State the blood parasite species.
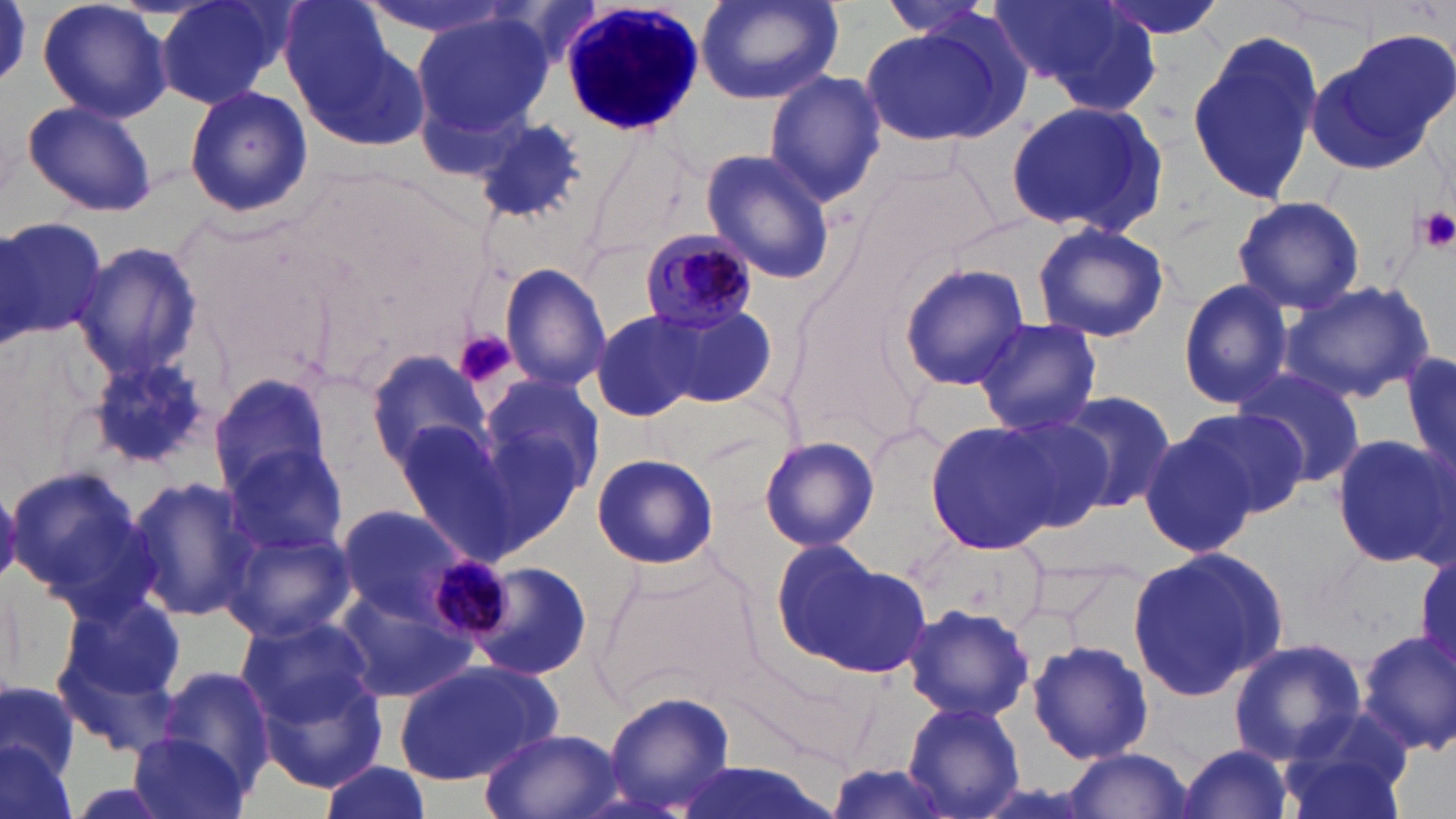

Plasmodium malariae.

field of view = single
magnification = 1000x
white blood cell locations = approximate bounding boxes as named x1/y1/x2/y2 corners in pixels: (x1=556, y1=1, x2=705, y2=140)
platelet locations = approximate bounding boxes as named x1/y1/x2/y2 corners in pixels: (x1=1415, y1=207, x2=1456, y2=254), (x1=455, y1=330, x2=516, y2=388)
preparation = thin blood smear
Plasmodium malariae-infected red blood cell locations = approximate bounding boxes as named x1/y1/x2/y2 corners in pixels: (x1=638, y1=228, x2=763, y2=335)
image size = 1456×819 pixels
uninfected red blood cell locations = approximate bounding boxes as named x1/y1/x2/y2 corners in pixels: (x1=37, y1=0, x2=173, y2=123), (x1=155, y1=0, x2=291, y2=108), (x1=696, y1=0, x2=844, y2=106), (x1=992, y1=0, x2=1161, y2=114), (x1=1093, y1=0, x2=1230, y2=43), (x1=874, y1=1, x2=1003, y2=38), (x1=411, y1=9, x2=554, y2=141), (x1=286, y1=10, x2=431, y2=149), (x1=858, y1=22, x2=1014, y2=150), (x1=1185, y1=27, x2=1322, y2=206), (x1=1310, y1=33, x2=1453, y2=174), (x1=763, y1=68, x2=887, y2=207), (x1=184, y1=86, x2=312, y2=215), (x1=22, y1=98, x2=156, y2=216), (x1=1005, y1=100, x2=1169, y2=238), (x1=468, y1=116, x2=588, y2=221), (x1=700, y1=150, x2=838, y2=285), (x1=853, y1=157, x2=997, y2=282), (x1=1231, y1=194, x2=1366, y2=316), (x1=0, y1=214, x2=106, y2=346), (x1=1032, y1=222, x2=1170, y2=343), (x1=72, y1=242, x2=203, y2=381), (x1=895, y1=262, x2=1030, y2=393), (x1=499, y1=263, x2=612, y2=391), (x1=1176, y1=278, x2=1297, y2=412), (x1=1281, y1=279, x2=1436, y2=403), (x1=662, y1=302, x2=775, y2=409), (x1=590, y1=311, x2=702, y2=423), (x1=975, y1=318, x2=1101, y2=435), (x1=366, y1=348, x2=493, y2=473), (x1=1401, y1=353, x2=1456, y2=480), (x1=87, y1=357, x2=214, y2=471), (x1=1235, y1=362, x2=1368, y2=489), (x1=208, y1=370, x2=334, y2=501), (x1=476, y1=370, x2=607, y2=511), (x1=1055, y1=391, x2=1174, y2=513), (x1=1182, y1=406, x2=1313, y2=519), (x1=987, y1=413, x2=1114, y2=535), (x1=390, y1=417, x2=517, y2=552), (x1=925, y1=420, x2=1060, y2=554), (x1=1137, y1=424, x2=1255, y2=561), (x1=1329, y1=432, x2=1455, y2=571), (x1=758, y1=434, x2=880, y2=553), (x1=222, y1=443, x2=349, y2=558), (x1=590, y1=453, x2=720, y2=571), (x1=4, y1=464, x2=154, y2=609), (x1=124, y1=476, x2=259, y2=622), (x1=334, y1=503, x2=476, y2=628), (x1=221, y1=524, x2=356, y2=641), (x1=913, y1=533, x2=1051, y2=638), (x1=772, y1=543, x2=930, y2=679), (x1=1123, y1=546, x2=1287, y2=705), (x1=464, y1=559, x2=594, y2=681), (x1=595, y1=560, x2=755, y2=713), (x1=333, y1=586, x2=482, y2=705), (x1=54, y1=591, x2=192, y2=738), (x1=903, y1=604, x2=1035, y2=722), (x1=233, y1=613, x2=376, y2=725), (x1=1354, y1=627, x2=1456, y2=755), (x1=1024, y1=637, x2=1157, y2=768), (x1=1229, y1=639, x2=1367, y2=762), (x1=392, y1=659, x2=560, y2=786), (x1=256, y1=664, x2=389, y2=794), (x1=155, y1=665, x2=277, y2=787), (x1=0, y1=680, x2=79, y2=791), (x1=603, y1=692, x2=738, y2=816), (x1=904, y1=700, x2=1025, y2=818), (x1=1274, y1=709, x2=1417, y2=819), (x1=479, y1=727, x2=622, y2=818), (x1=127, y1=729, x2=251, y2=819), (x1=0, y1=742, x2=76, y2=819), (x1=1175, y1=743, x2=1295, y2=819), (x1=1062, y1=747, x2=1195, y2=819), (x1=668, y1=759, x2=839, y2=819), (x1=317, y1=761, x2=433, y2=819)
modality = optical microscopy
stain = May-Grünwald-Giemsa